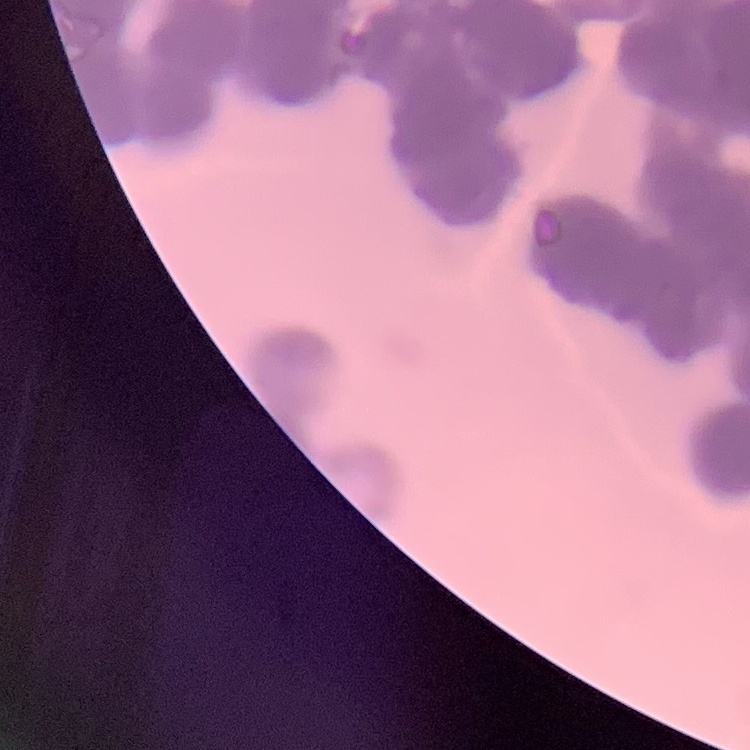

The red blood cells exhibit rouleaux formation. One tile cut from a larger photomicrograph. Field's or Giemsa stain. Thin blood smear.